Outline every parasitised red blood cell.
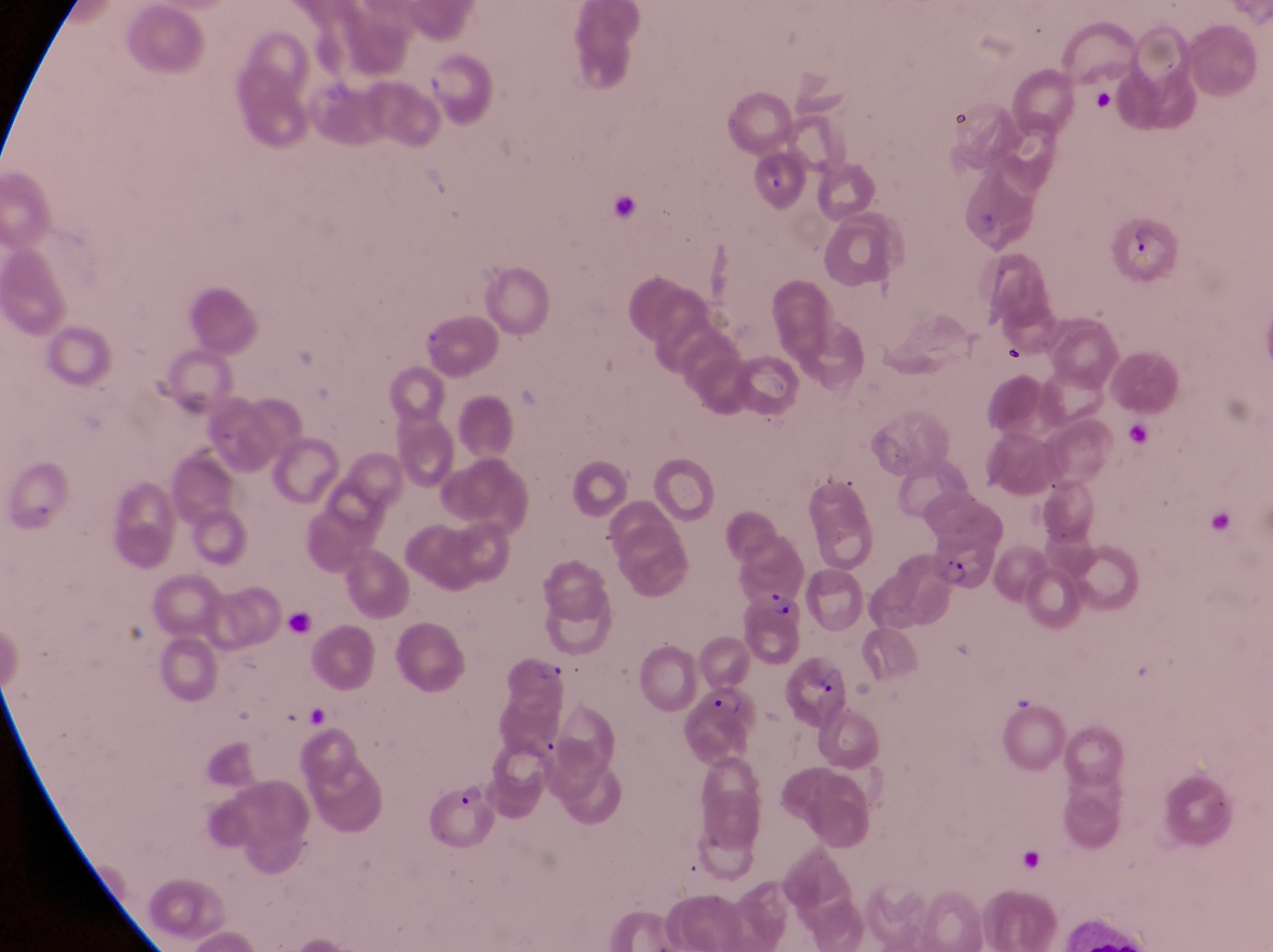

Approximate bounding boxes as left top right bottom in pixels.
Parasitised red blood cells: 1111 213 1181 281; 919 487 1002 592; 741 589 799 639; 494 639 569 714; 687 677 765 767; 421 784 498 852.

Summary:
  - Artifact (platelet-like body, stain precipitate, or debris) locations: 1096 85 1121 124; 999 339 1029 367; 784 644 849 731
  - Field of view: single
  - Country: Uganda
  - Preparation: thin blood smear
  - Capture: smartphone photograph through the eyepiece of an Olympus CX-23 microscope
  - Image size: 1273×952 pixels
  - Magnification: 1000x